Outline each Plasmodium malariae-infected red blood cell.
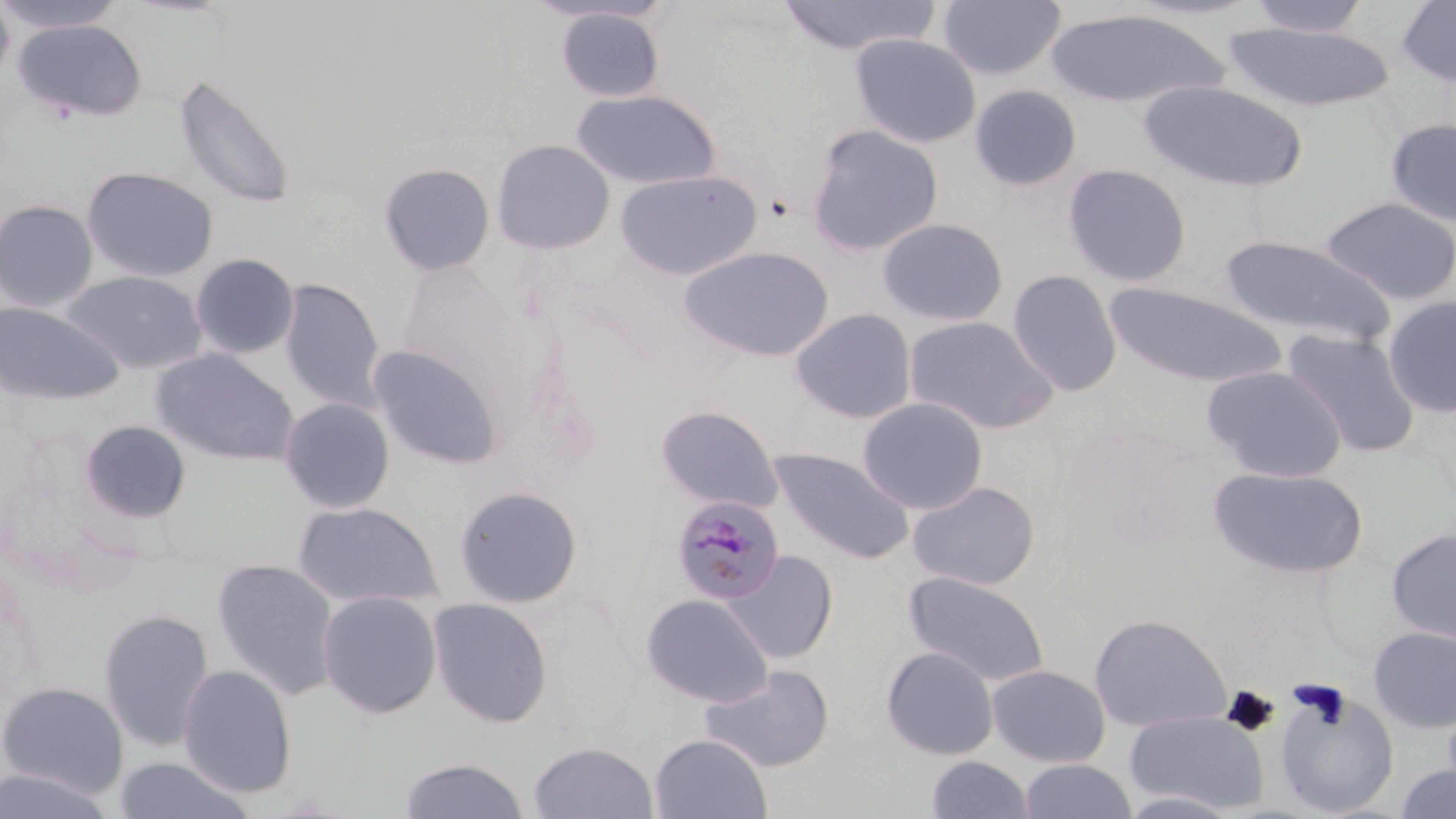
Approximate bounding boxes as (x1, y1, x2, y2) in pixels.
Plasmodium malariae-infected red blood cells: (670, 495, 786, 606).

Platelet locations: (1289, 679, 1353, 729), (1222, 686, 1279, 737). Uninfected red blood cell locations: (0, 0, 125, 34), (775, 0, 942, 57), (937, 0, 1066, 80), (1246, 0, 1372, 37), (1397, 0, 1456, 87), (0, 1, 15, 87), (555, 7, 665, 102), (1045, 8, 1229, 109), (15, 19, 147, 123), (1222, 23, 1395, 112), (849, 33, 981, 148), (173, 73, 297, 209), (1137, 79, 1309, 192), (970, 84, 1083, 190), (572, 89, 722, 189), (1385, 118, 1456, 228), (806, 124, 944, 255), (492, 140, 615, 254), (491, 155, 753, 259), (378, 162, 496, 276), (1063, 163, 1193, 287), (81, 166, 218, 283), (614, 169, 762, 280), (1320, 196, 1456, 306), (0, 198, 98, 313), (877, 217, 1009, 326), (1215, 234, 1396, 348), (679, 245, 834, 362), (190, 253, 299, 359), (1007, 269, 1123, 396), (61, 270, 208, 375), (279, 277, 387, 413), (1103, 280, 1287, 389), (1383, 295, 1456, 418), (0, 301, 124, 405), (791, 308, 917, 424), (904, 315, 1058, 434), (1282, 329, 1421, 458), (368, 346, 502, 469), (151, 348, 300, 466), (1201, 364, 1347, 482), (857, 396, 989, 514), (279, 397, 394, 513), (654, 404, 783, 513), (79, 420, 192, 522), (768, 447, 913, 564), (1207, 465, 1369, 579), (907, 481, 1040, 591), (454, 485, 583, 609), (293, 501, 444, 610), (1386, 526, 1456, 644), (722, 550, 839, 663), (212, 558, 340, 701), (903, 570, 1051, 688), (317, 590, 442, 719), (640, 593, 774, 707), (427, 597, 554, 728), (98, 608, 215, 752), (1089, 612, 1232, 732), (1369, 625, 1456, 733), (880, 645, 999, 760), (699, 663, 835, 772), (177, 664, 298, 799), (987, 664, 1110, 767), (0, 681, 129, 800), (1273, 686, 1401, 818), (1441, 695, 1456, 800), (1125, 709, 1269, 814), (649, 733, 773, 819), (529, 739, 658, 819), (398, 756, 529, 818), (926, 756, 1034, 818), (112, 757, 258, 818), (1018, 759, 1137, 818), (1392, 763, 1456, 819), (0, 768, 118, 818), (1114, 790, 1247, 819). Slide-level diagnosis: Plasmodium malariae. One field of a larger specimen. May-Grünwald-Giemsa stain. Image is 1456×819 pixels. Thin blood film. Optical microscopy. 1000x magnification.